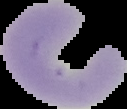

Summary:
  - Malaria status: uninfected
  - Image type: segmented cell region with the area outside set to black
  - Image size: 127×109 pixels
  - Preparation: thin blood film